Classify this cell by malaria status.
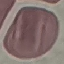
Uninfected.

Automatically extracted cell patch, resized to 64 × 64 pixels. Giemsa-stained preparation. Photographed with a smartphone camera at the microscope eyepiece. Thin smear of blood.